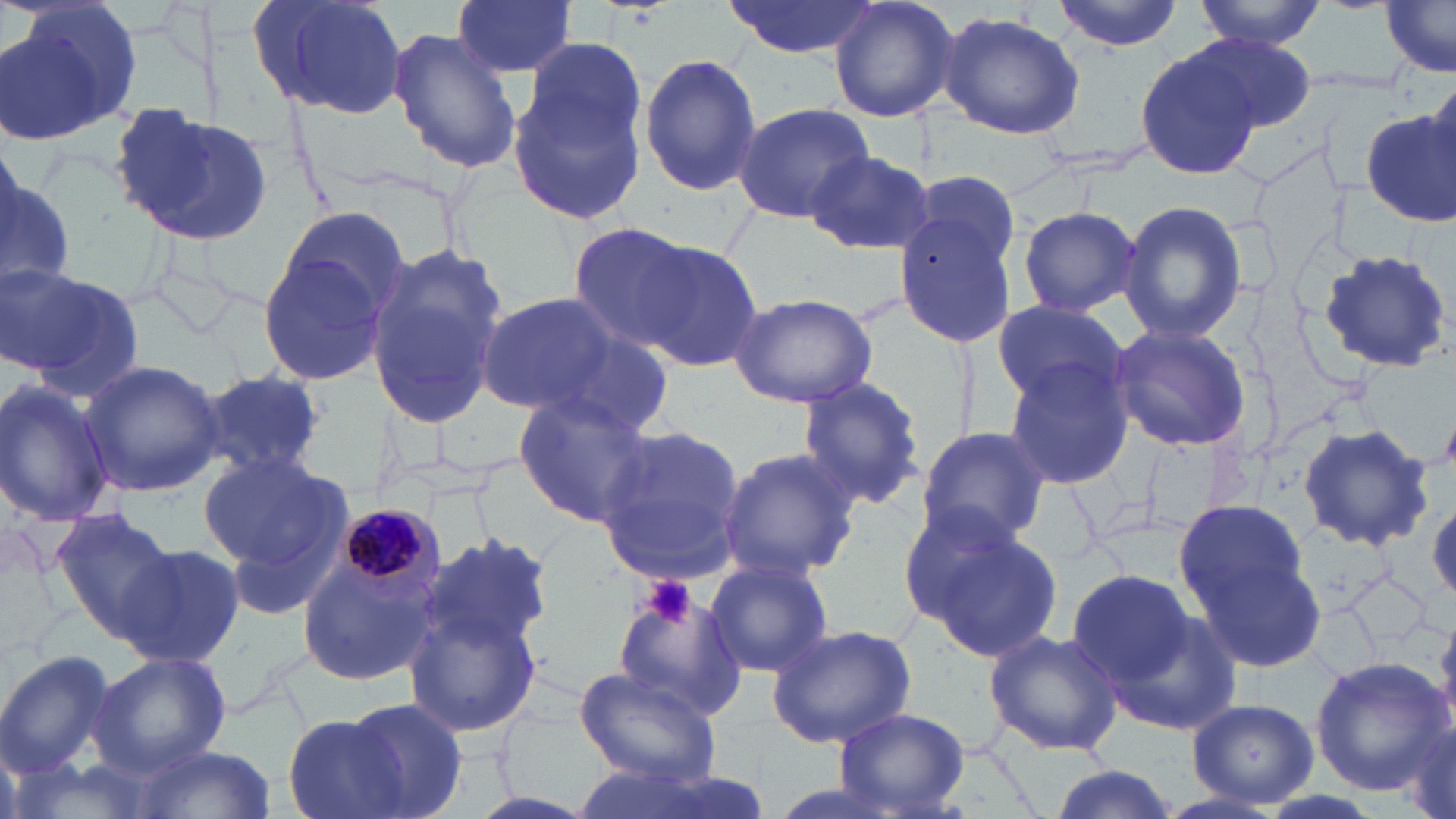
Summary:
  - Coordinate format: approximate bounding boxes as (x1,y1)-(x2,y2) corner pairs in pixels
  - Plasmodium malariae-infected red blood cell locations: (330,505)-(444,610)
  - Uninfected red blood cell locations: (2,0)-(146,145), (245,0)-(409,117), (451,0)-(577,80), (725,0)-(879,59), (828,0)-(960,123), (1054,0)-(1181,51), (1195,0)-(1324,49), (1380,1)-(1456,75), (938,11)-(1084,139), (387,27)-(522,174), (1186,33)-(1316,136), (522,39)-(649,155), (1134,45)-(1261,181), (638,52)-(762,196), (508,63)-(649,225), (733,103)-(877,223), (114,104)-(273,246), (1358,105)-(1455,223), (805,149)-(935,256), (0,165)-(75,297), (907,170)-(1022,276), (1119,201)-(1246,343), (275,204)-(415,326), (1017,206)-(1142,316), (894,208)-(1019,349), (567,223)-(702,352), (636,239)-(762,371), (255,240)-(392,389), (361,245)-(509,423), (1317,248)-(1451,374), (3,268)-(144,398), (476,292)-(638,421), (729,292)-(879,408), (990,298)-(1130,409), (1108,324)-(1250,451), (534,328)-(676,440), (1003,359)-(1134,490), (76,360)-(226,500), (191,365)-(328,487), (797,376)-(925,509), (0,381)-(117,529), (513,395)-(657,529), (1296,424)-(1433,550), (596,425)-(744,584), (914,426)-(1052,551), (718,446)-(859,582), (197,453)-(344,578), (898,496)-(1031,618), (1173,498)-(1319,651), (51,507)-(182,639), (926,526)-(1063,664), (405,529)-(552,727), (118,542)-(246,669), (294,553)-(434,687), (703,556)-(835,679), (1067,570)-(1196,687), (613,584)-(745,723), (1103,608)-(1241,734), (1429,611)-(1456,742), (766,623)-(917,749), (984,628)-(1123,755), (0,650)-(118,774), (91,650)-(230,775), (1309,659)-(1450,793), (574,665)-(722,786), (344,697)-(470,819), (1186,698)-(1318,807), (835,707)-(970,816), (282,713)-(410,819), (1397,715)-(1455,819), (129,744)-(275,819), (1044,766)-(1181,819)
  - Platelet locations: (640,574)-(697,631)
  - Slide-level diagnosis: Plasmodium malariae
  - Magnification: 1000x
  - Field of view: single
  - Stain: May-Grünwald-Giemsa
  - Image size: 1456×819 pixels
  - Modality: optical microscopy
  - Preparation: thin blood film